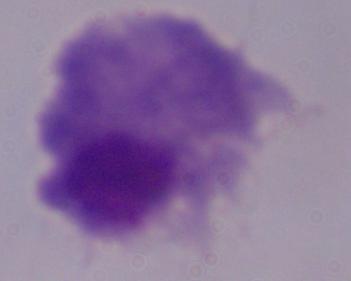

Captured at 1000x magnification. A trichomonad is seen. Micrograph.